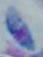
Toxoplasma gondii is seen. 1000x magnification. Micrograph.